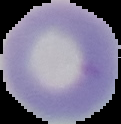

image_type: cell region segmented out of the field of view; surrounding area masked to black
image_size: 121×124 pixels
preparation: thin blood smear
result: negative for malaria parasites